Identify the parasite.
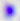
This is Toxoplasma gondii.

Summary:
  - Modality: photomicrograph
  - Magnification: 400x